Report the malaria status of this cell.
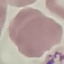
It is parasitized.

Summary:
  - Image type: cell patch, automatically extracted from a larger field of view and resized to 64 × 64 pixels
  - Capture: smartphone camera at the microscope eyepiece
  - Preparation: thin blood film
  - Stain: Giemsa